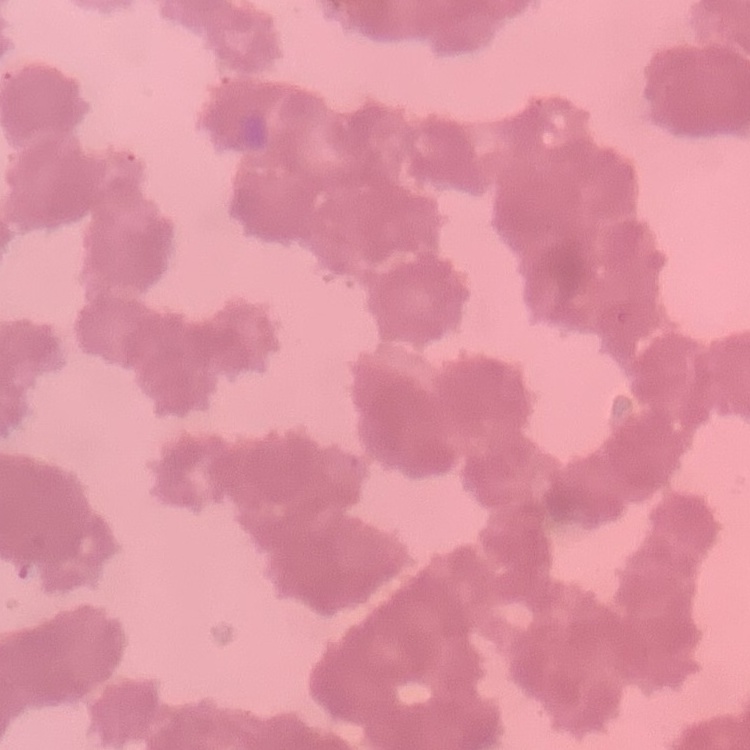

Summary:
  - Erythrocyte morphology: rouleaux formation
  - Stain: Field's or Giemsa
  - Preparation: thin blood smear
  - Image type: one tile cut from a larger photomicrograph